Identify the parasite.
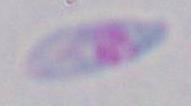
Toxoplasma gondii.

1000x magnification. Micrograph.